Assess this cell for malaria.
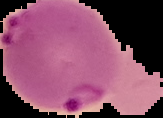
Parasitized.

image type = segmented cell region with the area outside set to black
image size = 163×118 pixels
preparation = thin blood film